Give the extent of all Plasmodium falciparum-infected red blood cells.
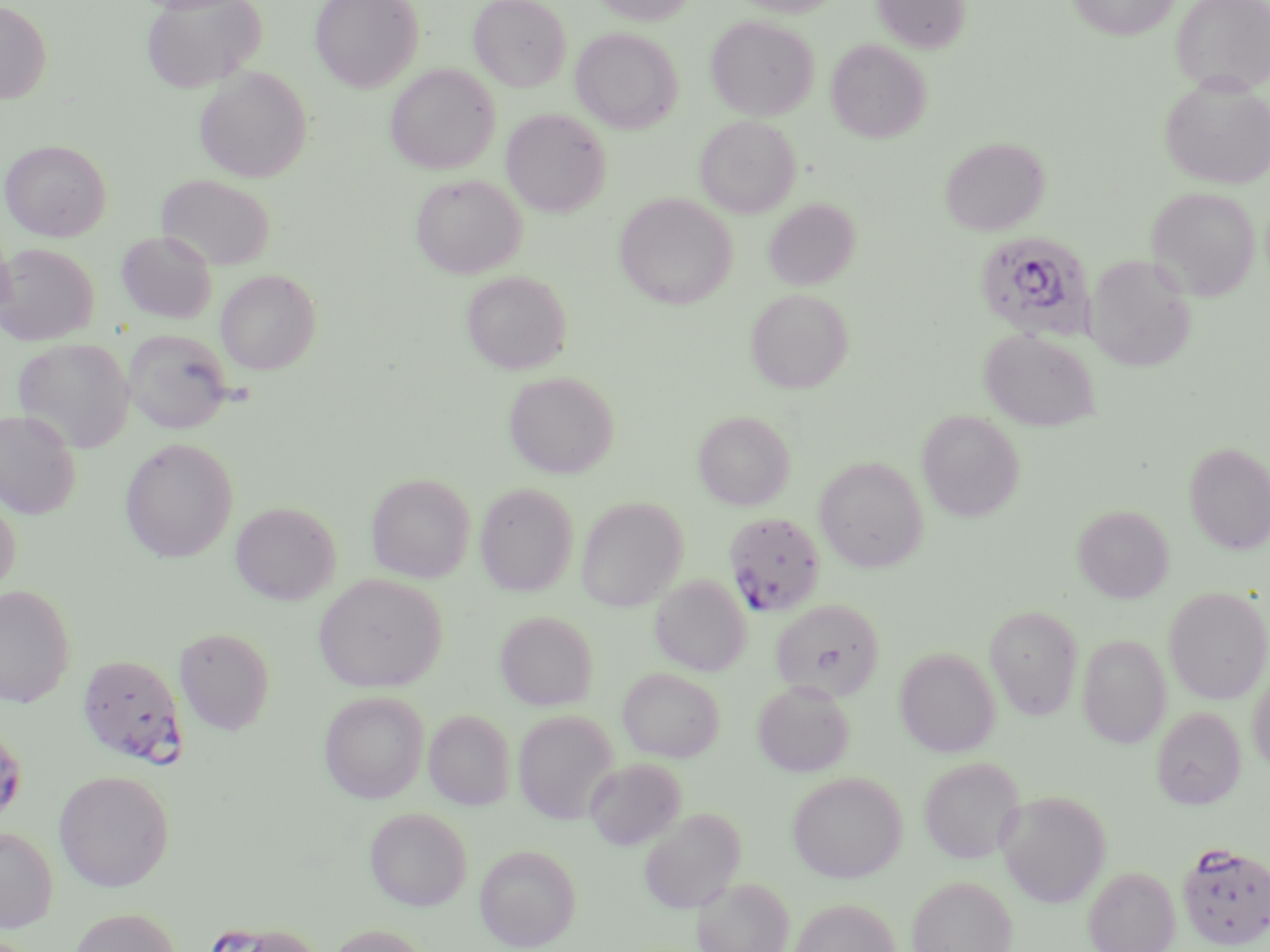

Approximate bounding boxes as (x1, y1, x2, y2) in pixels.
Plasmodium falciparum-infected red blood cells: (974, 231, 1095, 340), (724, 512, 826, 617), (78, 654, 186, 765), (0, 729, 30, 820), (1177, 842, 1270, 950), (206, 918, 322, 952).

slide-level diagnosis = Plasmodium falciparum
stain = May-Grünwald-Giemsa
modality = light microscopy
magnification = 1000x
preparation = thin blood smear
field of view = one of a larger specimen
uninfected red blood cell locations = approximate bounding boxes as (x1, y1, x2, y2) in pixels: (140, 0, 265, 93), (310, 0, 423, 92), (470, 0, 571, 91), (592, 0, 696, 26), (729, 0, 844, 17), (872, 0, 970, 53), (1068, 0, 1179, 40), (1171, 0, 1270, 95), (0, 2, 52, 104), (705, 15, 819, 120), (571, 27, 683, 134), (826, 38, 931, 143), (384, 64, 500, 174), (194, 66, 312, 183), (1160, 76, 1270, 190), (501, 109, 610, 217), (694, 115, 800, 218), (940, 136, 1050, 235), (1, 139, 111, 241), (156, 174, 276, 269), (411, 174, 527, 278), (1146, 186, 1260, 301), (614, 193, 736, 310), (763, 199, 860, 291), (116, 231, 218, 324), (0, 243, 99, 345), (1084, 254, 1197, 371), (216, 269, 321, 374), (461, 270, 572, 375), (745, 288, 853, 394), (123, 328, 234, 434), (979, 328, 1100, 431), (13, 338, 136, 454), (504, 371, 619, 479), (917, 409, 1024, 522), (0, 410, 82, 518), (693, 411, 795, 511), (119, 437, 238, 564), (1184, 442, 1270, 555), (814, 456, 928, 572), (367, 473, 475, 583), (475, 482, 579, 596), (0, 490, 21, 595), (576, 497, 687, 612), (231, 501, 340, 605), (1073, 504, 1174, 603), (314, 573, 446, 692), (650, 576, 750, 676), (0, 585, 76, 708), (1164, 587, 1270, 704), (770, 599, 884, 701), (985, 605, 1082, 720), (495, 610, 598, 710), (175, 626, 275, 735), (1077, 634, 1171, 749), (895, 646, 1000, 757), (618, 667, 725, 762), (1247, 669, 1270, 774), (752, 680, 855, 778), (319, 691, 429, 803), (1151, 707, 1245, 810), (424, 709, 515, 810), (513, 710, 619, 825), (919, 756, 1025, 864), (584, 757, 686, 851), (53, 770, 174, 891), (787, 771, 908, 883), (996, 790, 1111, 907), (364, 806, 472, 911), (638, 807, 746, 914), (0, 827, 58, 932), (475, 844, 581, 950), (1083, 865, 1180, 952), (907, 875, 1018, 952), (693, 876, 794, 952), (788, 897, 901, 952), (67, 907, 183, 952), (327, 924, 433, 952)
image size = 1270×952 pixels